Classify this cell by malaria status.
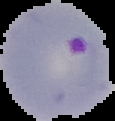
It is parasitized.

Summary:
  - Preparation: thin blood film
  - Image type: segmented cell region with the area outside set to black
  - Image size: 115×121 pixels